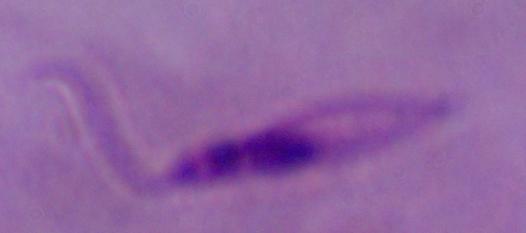

identification = Leishmania
modality = photomicrograph
magnification = 1000x